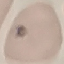

Summary:
  - Result: no malaria parasites seen
  - Capture: smartphone through the microscope eyepiece
  - Preparation: thin smear
  - Stain: Giemsa
  - Image type: automatically extracted cell patch, resized to 64 × 64 pixels